Report the malaria status of this cell.
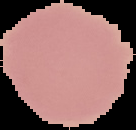

It is uninfected.

Image is 136×130 pixels. From a thin blood film. The area outside the segmented cell region is set to black.